Assess the morphology of the erythrocytes.
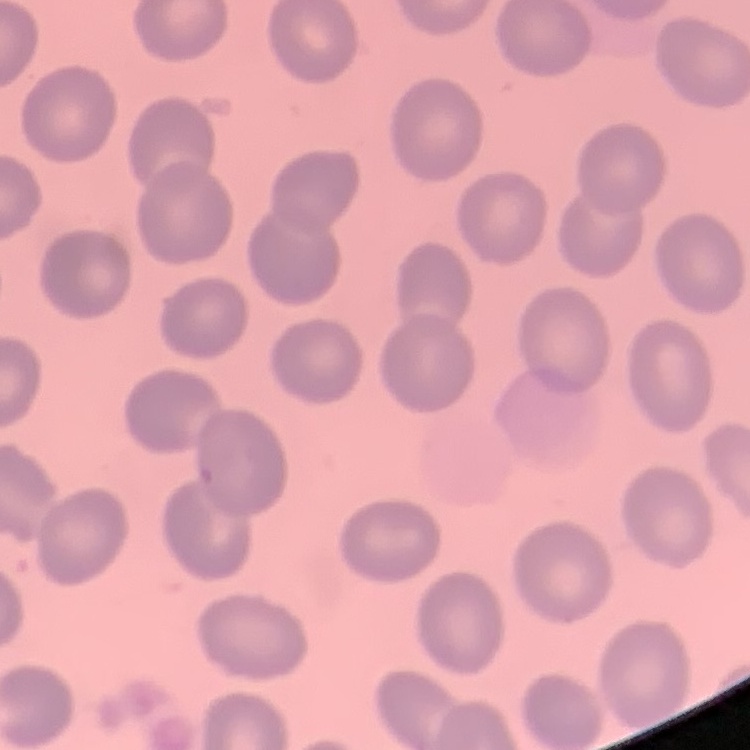

No rouleaux formation.

Field's or Giemsa stain. Thin blood film. Square crop of a larger photomicrograph.